Assess this cell for malaria.
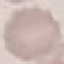

It is uninfected.

Thin blood smear. Automatically extracted cell patch, resized to 64 × 64 pixels. Photographed with a smartphone camera at the microscope eyepiece. Giemsa-stained preparation.